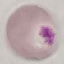

result = negative for malaria parasites
preparation = thin smear
image type = automatically extracted cell patch, resized to 64 × 64 pixels
capture = smartphone through the microscope eyepiece
stain = Giemsa